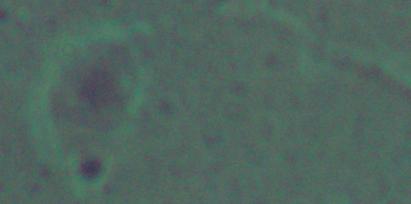
Captured at 1000x magnification. Micrograph. A Leishmania parasite is shown.